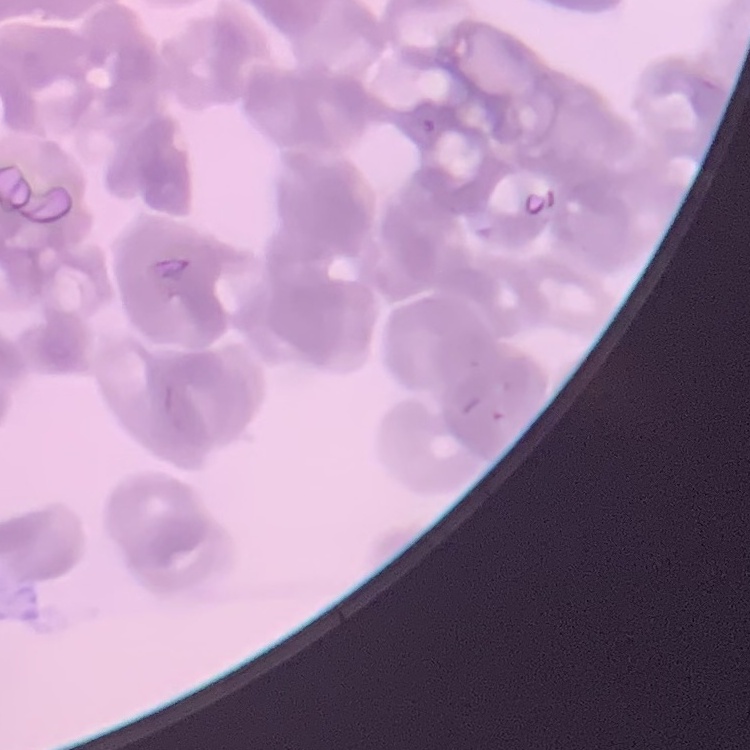
Summary:
  - Erythrocyte morphology: rouleaux formation
  - Image type: one tile cut from a larger photomicrograph
  - Stain: Field's or Giemsa
  - Preparation: thin blood smear